Assess this cell for malaria.
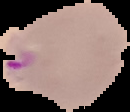

It is parasitized.

From a thin blood smear. Cell region segmented out of the field of view; the surrounding area is masked to black. Image is 130×112 pixels.